Describe the morphology of the erythrocytes.
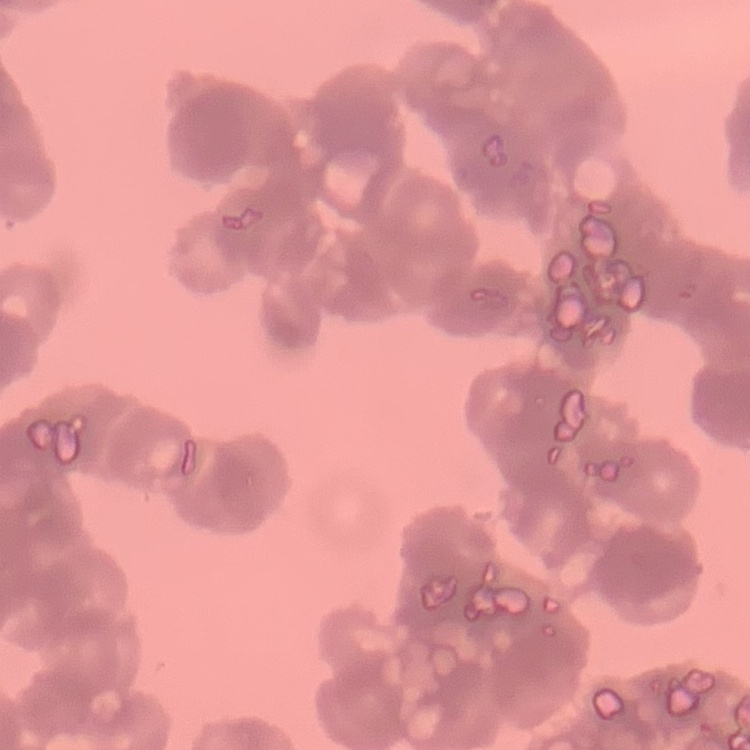

Rouleaux formation.

stain: Field's or Giemsa
preparation: thin blood film
image_type: square crop of a larger photomicrograph